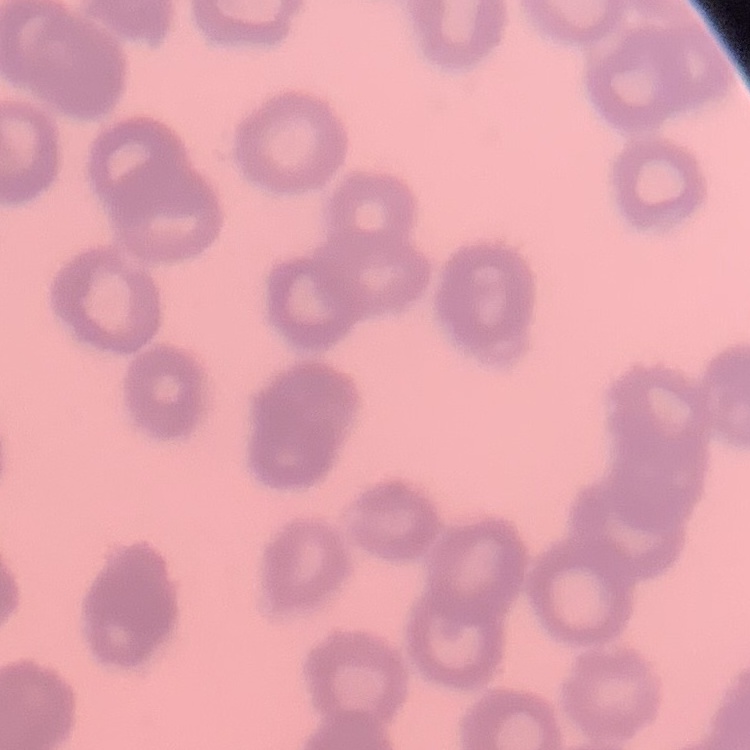

The erythrocytes exhibit rouleaux formation. Stained with either Field's or Giemsa. Thin blood smear. Square crop of a larger photomicrograph.